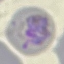
{
  "malaria_status": "parasitized",
  "stain": "Giemsa",
  "capture": "smartphone camera at the microscope eyepiece",
  "image_type": "automatically extracted cell patch, resized to 64 × 64 pixels",
  "preparation": "thin blood smear"
}